State which parasite is depicted.
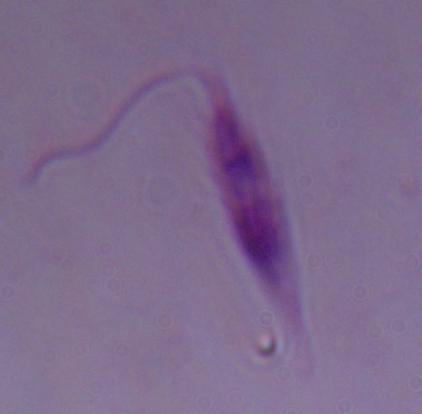

Leishmania.

Summary:
  - Magnification: 1000x
  - Modality: micrograph